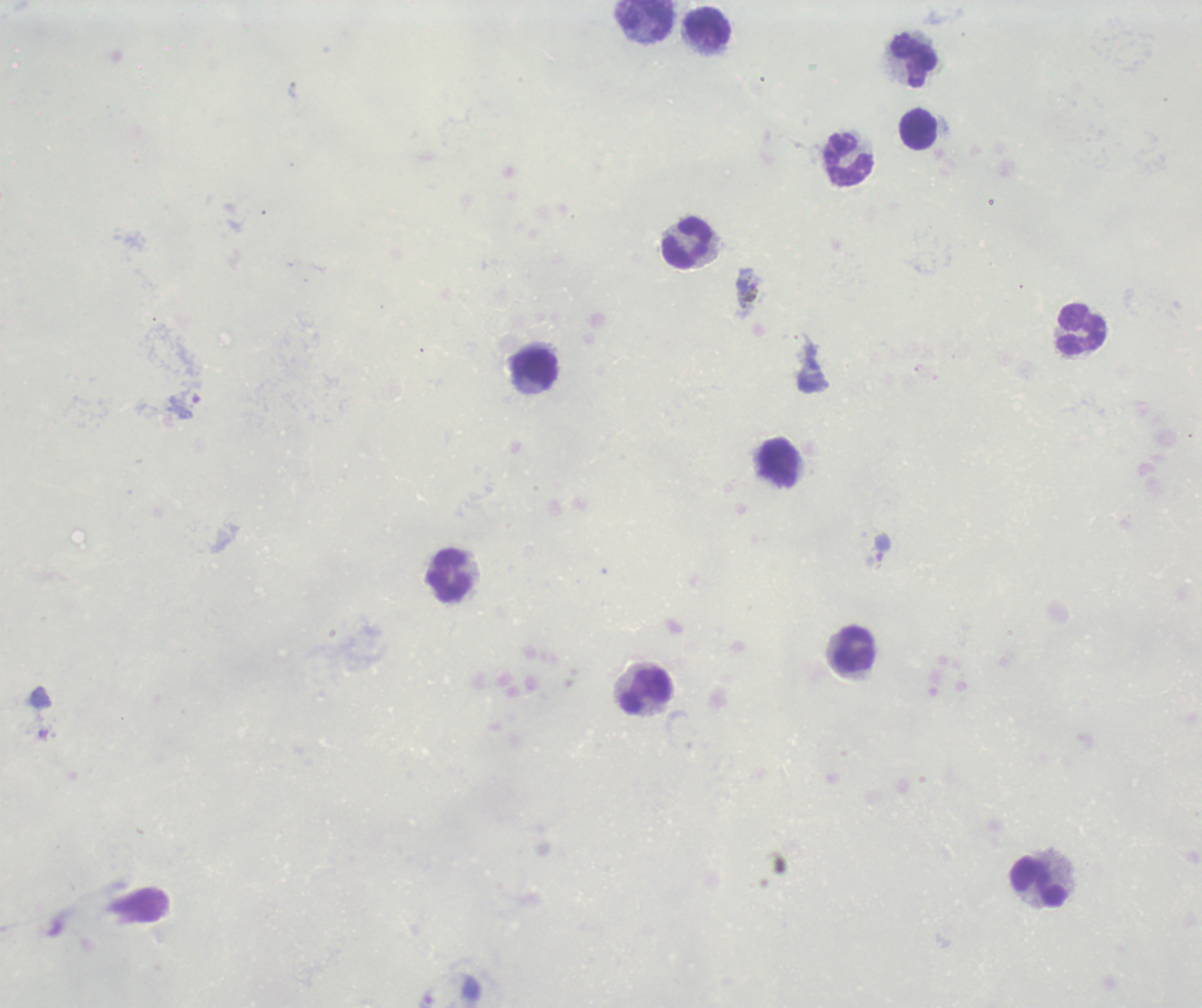 Approximate centers as [x, y] in pixels. Trophozoite locations: [883, 547]. Leukocyte locations: [646, 19], [707, 27], [914, 61], [919, 130], [850, 159], [687, 244], [1081, 330], [536, 368], [779, 463], [449, 575], [854, 650], [648, 691], [1040, 883]. Gametocyte locations: [747, 293]. Life-cycle stages observed: trophozoite, gametocyte. Thick smear of blood. Background quality: unsatisfactory. Result: malaria parasites detected. Previously used in an actual diagnosis. Image is 1202×1008 pixels. Single field of view. 100x magnification. Romanowsky stain.